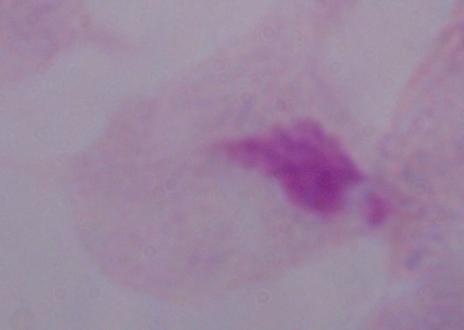

Summary:
  - Magnification: 1000x
  - Identification: trichomonad
  - Modality: photomicrograph